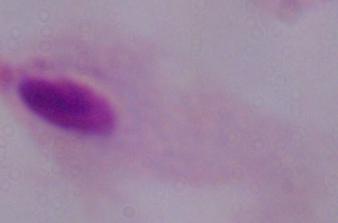
magnification = 1000x
modality = micrograph
identification = trichomonad